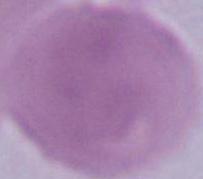
magnification = 1000x
identification = red blood cell
modality = micrograph